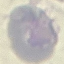
Summary:
  - Result: no malaria parasites detected
  - Capture: smartphone camera at the microscope eyepiece
  - Preparation: thin blood film
  - Stain: Giemsa
  - Image type: automatically extracted cell patch, resized to 64 × 64 pixels